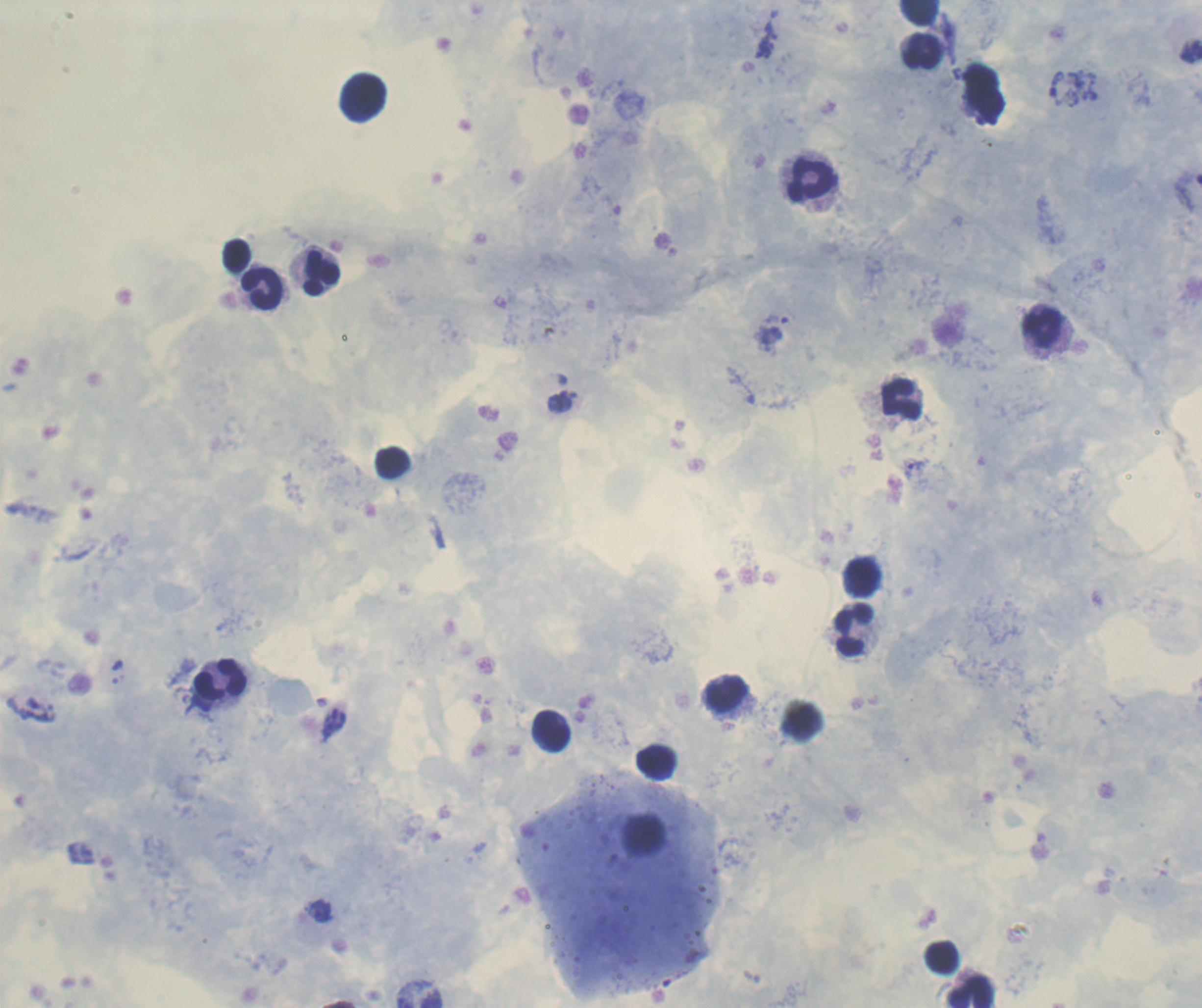
Approximate centers as [x, y] in pixels.
Summary:
  - Trophozoite locations: [771, 31], [768, 44], [763, 53], [560, 401], [914, 469], [320, 911]
  - Leukocyte locations: [922, 14], [923, 54], [362, 99], [809, 182], [237, 256], [317, 272], [262, 290], [1044, 327], [899, 403], [394, 465], [863, 577], [855, 631], [220, 682], [725, 694], [549, 733], [657, 763], [941, 957], [971, 991]
  - Preparation: thick blood smear
  - Coloration quality: good
  - Field of view: one from this slide
  - Stain: Romanowsky
  - Result: positive for malaria parasites
  - Context: previously used in a real diagnosis
  - Magnification: 100x
  - Image size: 1202×1008 pixels
  - Background quality: good